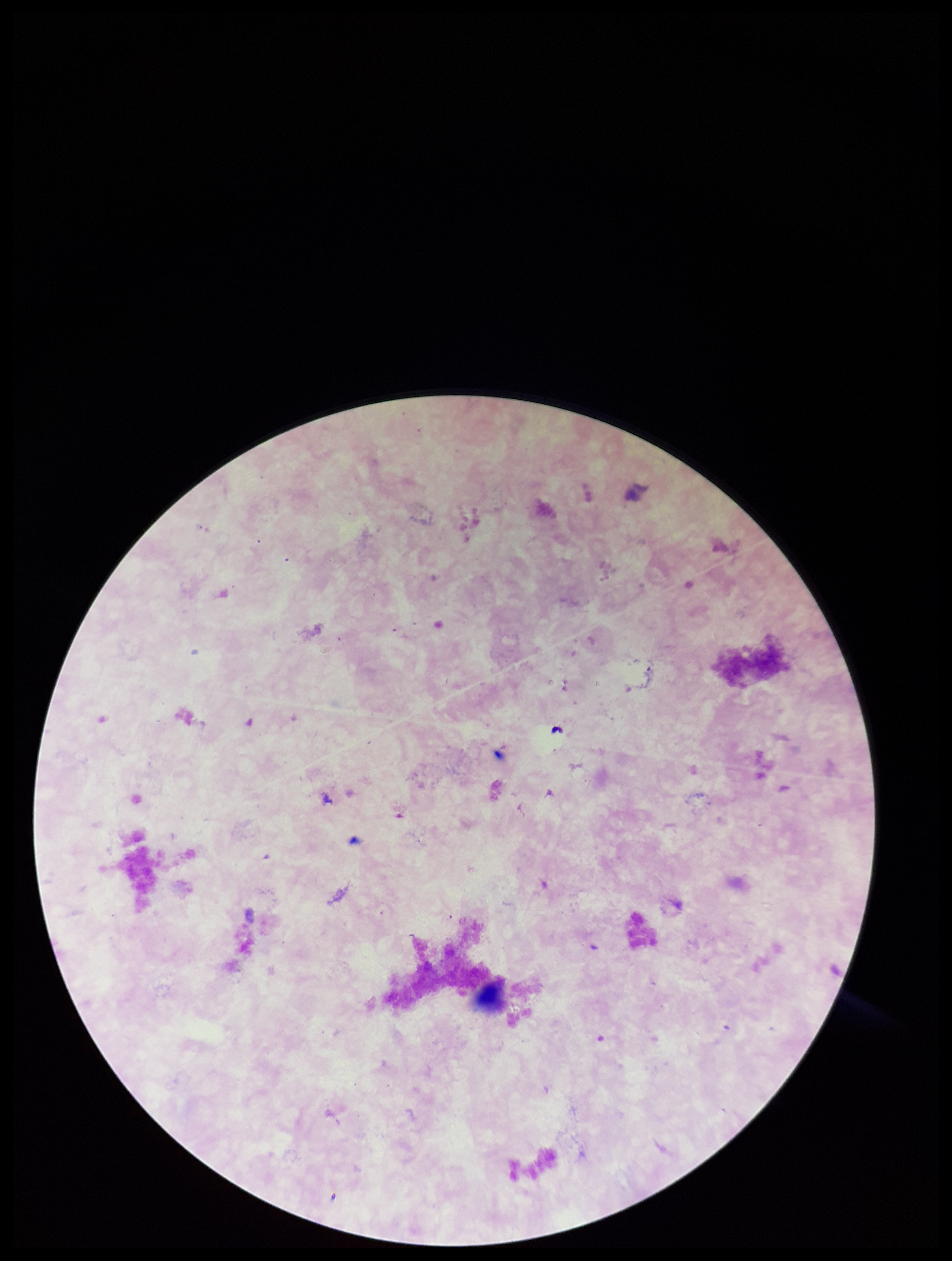
Plasmodium parasites: none identified. Leukocyte count: 0. Parasite count: 0. Patient malaria status: negative. Preparation: thick blood smear. Image is 952×1261 pixels. Stained with Giemsa. One field from this slide. Photographed through the microscope eyepiece with a smartphone camera.